Describe the morphology of the erythrocytes.
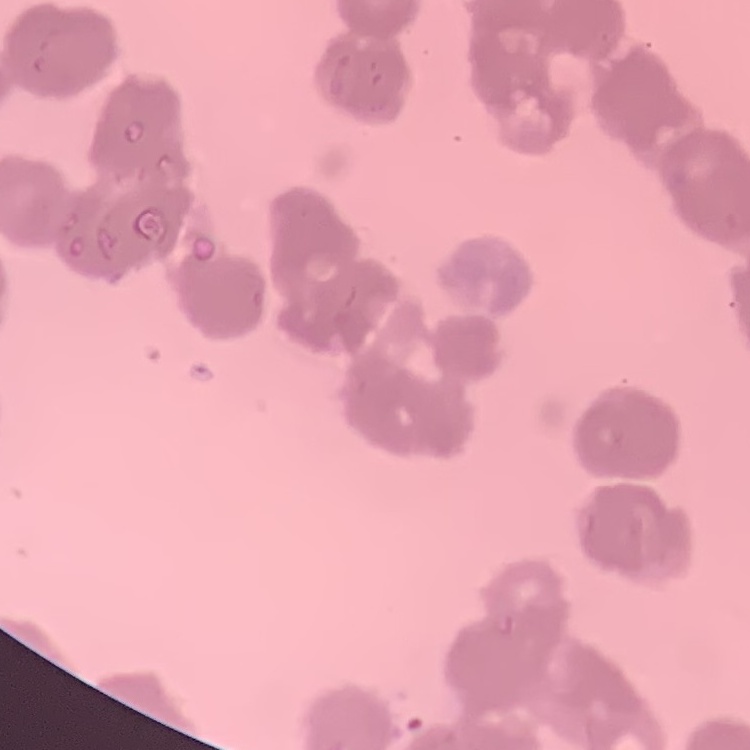

They show rouleaux formation.

Summary:
  - Image type: square crop of a larger photomicrograph
  - Preparation: thin blood smear
  - Stain: Field's or Giemsa